Name the cell type shown.
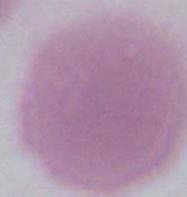
An erythrocyte.

Micrograph. 1000x magnification.